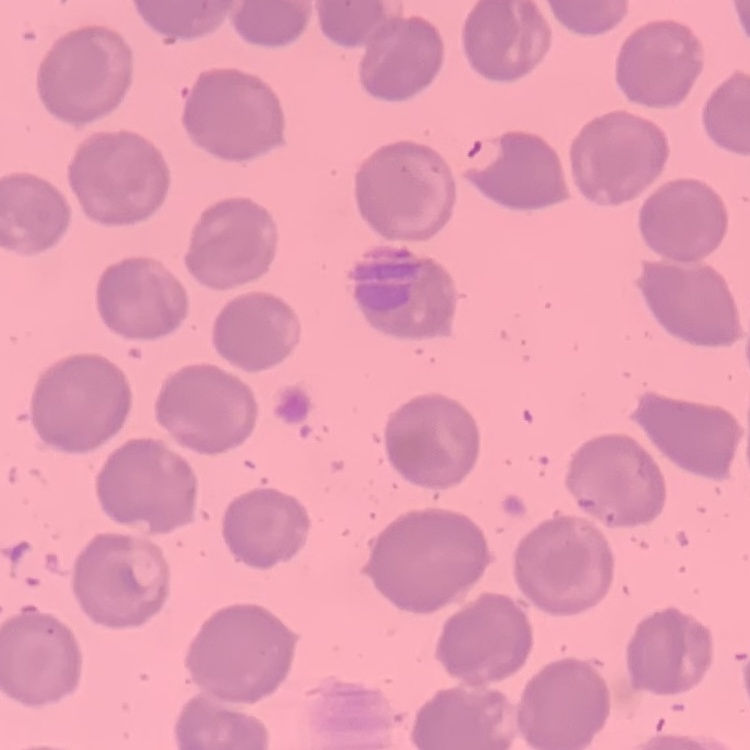
erythrocyte morphology = no rouleaux formation
stain = Field's or Giemsa
image type = square crop of a larger photomicrograph
preparation = thin blood film